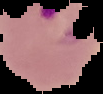
image size = 103×94 pixels
image type = cell region segmented out of the field of view; surrounding area masked to black
malaria status = parasitized
preparation = thin blood film